Assess this cell for malaria.
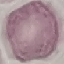
It is uninfected.

Thin blood film. Cell patch, automatically extracted from a larger field of view and resized to 64 × 64 pixels. Giemsa-stained preparation. Photographed with a smartphone camera at the microscope eyepiece.